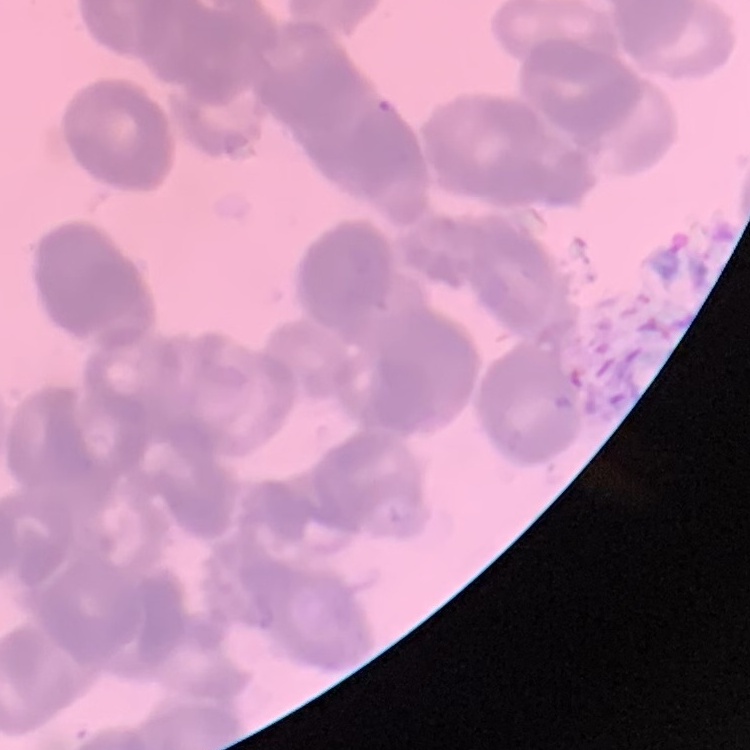

Summary:
  - Erythrocyte morphology: rouleaux formation
  - Preparation: thin blood smear
  - Image type: one tile cut from a larger photomicrograph
  - Stain: Field's or Giemsa